Point out Plasmodium parasites and leukocytes.
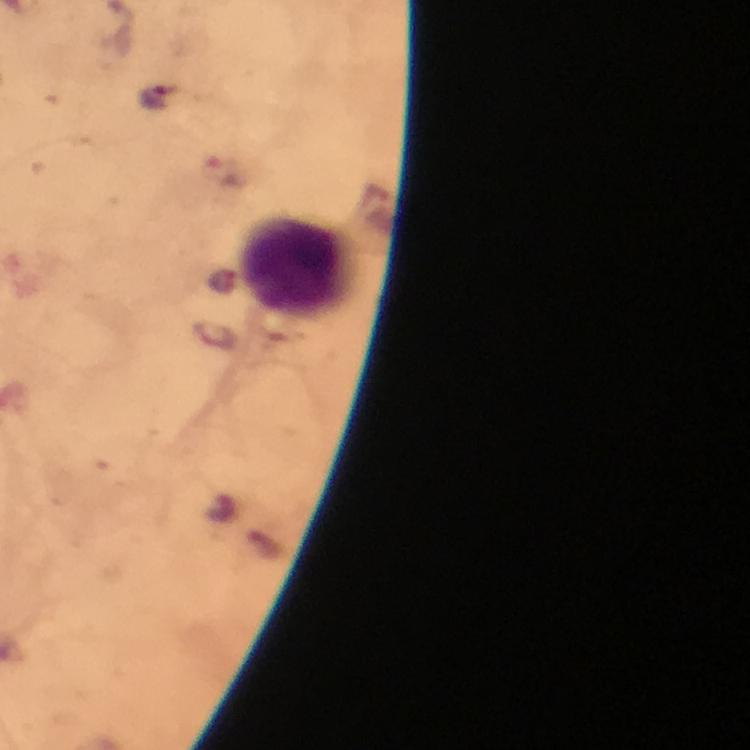

No Plasmodium parasites seen.
Approximate centers as (x, y) in pixels.
Leukocytes: (295, 268).

Photographed with a smartphone mounted on the microscope. Giemsa stain. From a diagnostic examination for malaria. A crop from one field of view. Immersion oil applied. Thick blood smear. Image is 750×750 pixels. 100x magnification.